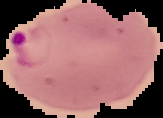
preparation = thin blood film
image size = 163×118 pixels
malaria status = parasitized
image type = segmented cell region with the area outside set to black